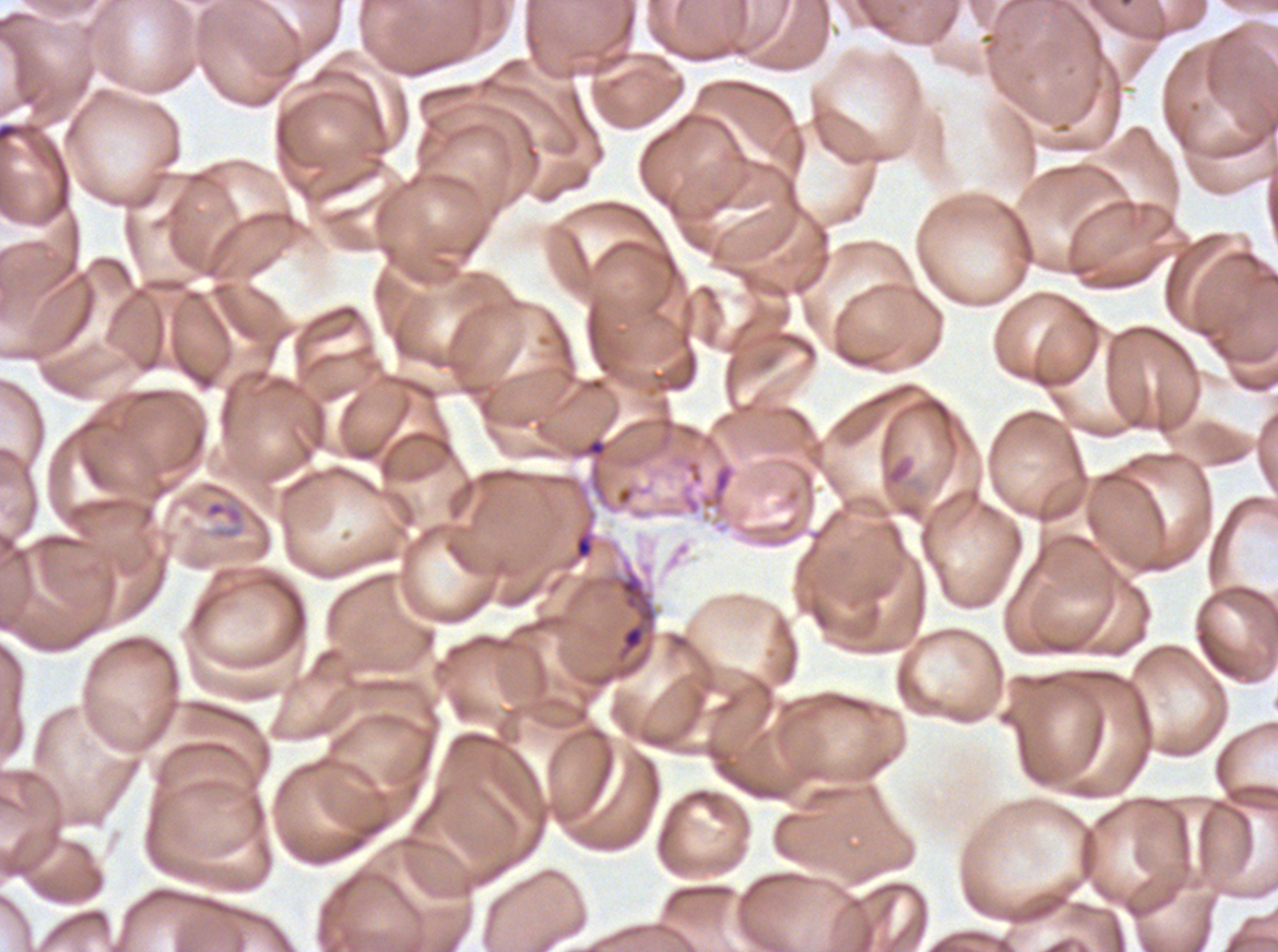
debris_locations: 'approximate bounding boxes as [x1, y1, x2, y2] in pixels: [582, 436, 608, 458], [573, 532, 595, 560], [614, 567, 657, 665]'
field_of_view: sub-image separated from a larger composite
stain: Giemsa
preparation: thin blood film
image_size: 1278×952 pixels
specimen: P. falciparum from a patient in The Gambia, cultured ex vivo for 24 to 48 hours
ring_locations: 'approximate bounding boxes as [x1, y1, x2, y2] in pixels: [203, 498, 245, 540]'